Give the position of every malaria parasite.
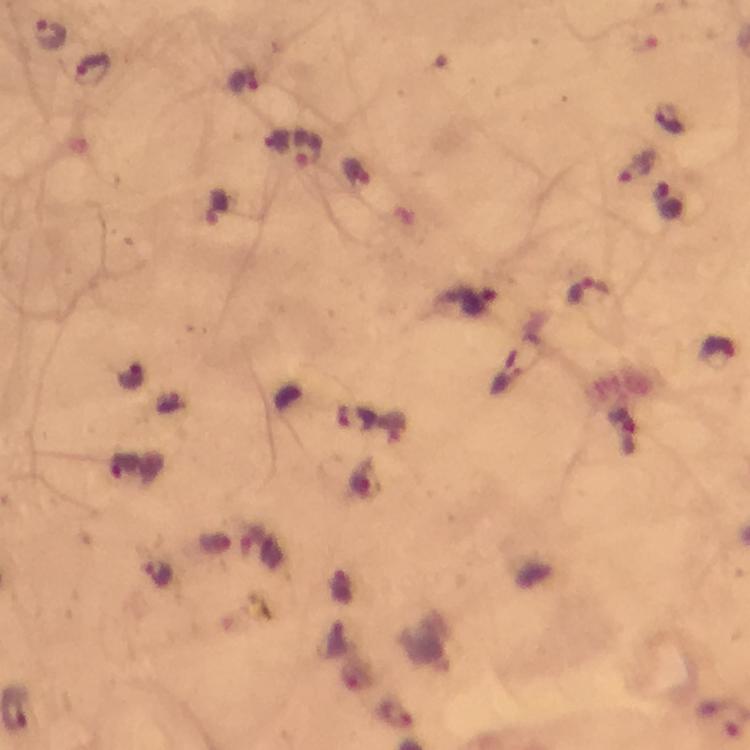
Approximate centers as {x, y} in pixels.
Malaria parasites: {51, 33}, {91, 69}, {243, 83}, {666, 118}, {307, 148}, {634, 165}, {354, 174}, {669, 200}, {588, 290}, {475, 298}, {717, 349}, {353, 419}, {622, 432}, {158, 573}.

capture = smartphone mounted on the microscope
magnification = 100x
cropped from = one field of view
immersion oil = applied
preparation = thick blood smear
image size = 750×750 pixels
context = from a malaria diagnostic workup
stain = Giemsa